Find each parasitized red blood cell.
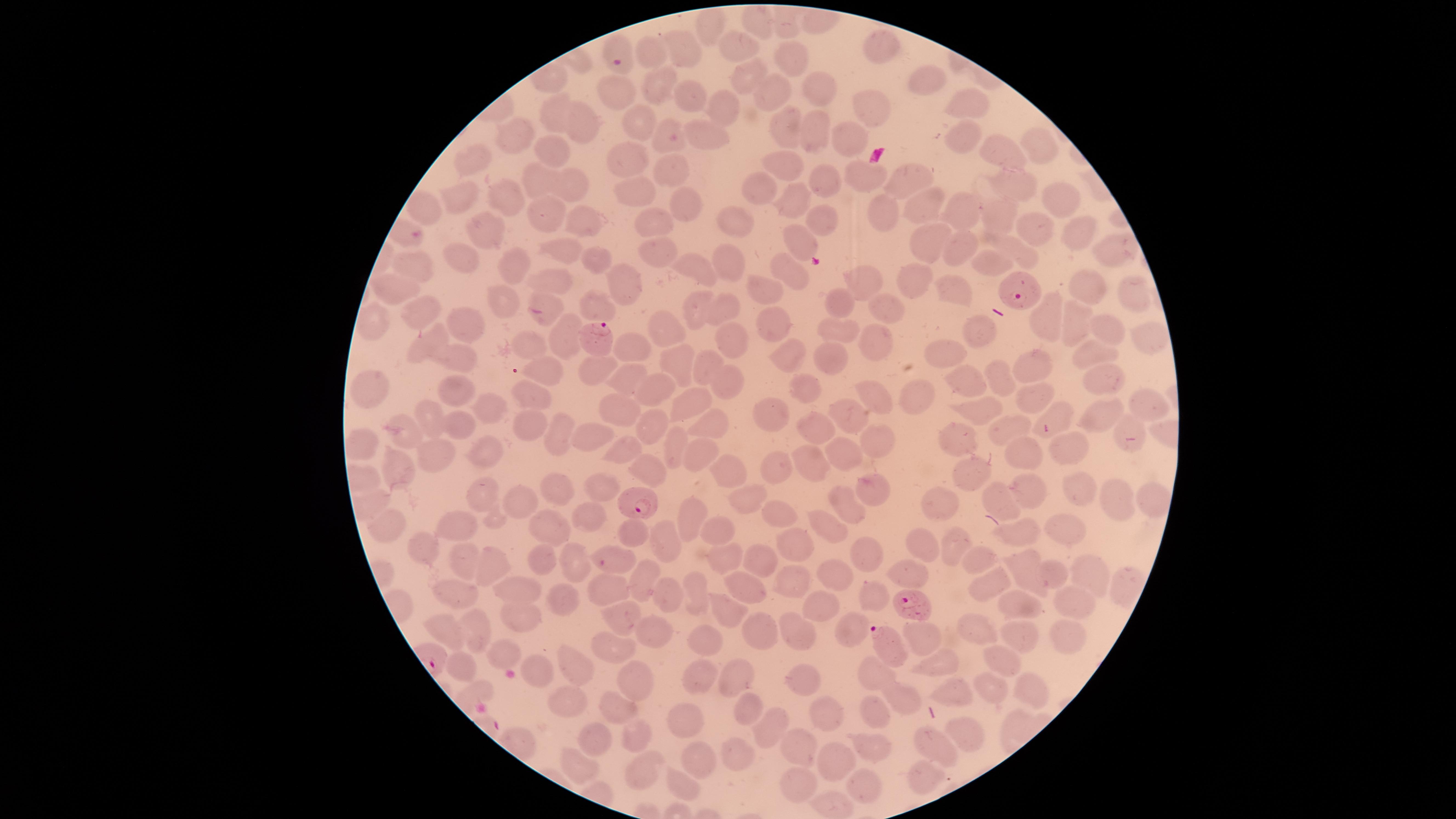

Approximate marker points as {x, y} in pixels.
Parasitized red blood cells: {621, 57}, {1019, 291}, {602, 335}, {643, 506}, {913, 602}, {883, 642}.

preparation: thin smear of blood
field_of_view: single
visible_region: circular
stain: Giemsa
image_size: 1456×819 pixels
species: Plasmodium falciparum
uninfected_red_blood_cells: 'approximate marker points as {x, y} in pixels: {760, 23}, {708, 24}, {734, 44}, {678, 48}, {876, 49}, {655, 56}, {792, 56}, {744, 77}, {658, 79}, {918, 81}, {774, 87}, {821, 90}, {615, 93}, {687, 99}, {721, 105}, {971, 105}, {549, 111}, {875, 113}, {584, 125}, {638, 126}, {784, 126}, {815, 132}, {518, 135}, {670, 135}, {705, 135}, {846, 140}, {962, 142}, {1043, 148}, {551, 150}, {1002, 151}, {472, 156}, {631, 157}, {671, 165}, {779, 165}, {861, 172}, {908, 173}, {1012, 179}, {535, 180}, {575, 182}, {825, 183}, {757, 189}, {640, 192}, {685, 195}, {503, 197}, {466, 198}, {796, 198}, {1057, 202}, {424, 207}, {925, 208}, {962, 210}, {884, 215}, {552, 217}, {649, 218}, {996, 218}, {580, 222}, {823, 222}, {737, 224}, {479, 230}, {1032, 230}, {1078, 236}, {928, 241}, {960, 243}, {803, 244}, {1111, 247}, {463, 252}, {563, 252}, {1024, 252}, {661, 253}, {596, 256}, {729, 259}, {990, 259}, {509, 262}, {414, 266}, {693, 266}, {796, 270}, {553, 282}, {757, 282}, {915, 283}, {623, 284}, {401, 285}, {872, 285}, {1083, 285}, {952, 290}, {1126, 293}, {501, 300}, {418, 302}, {690, 302}, {837, 303}, {723, 304}, {887, 309}, {595, 310}, {547, 312}, {1048, 314}, {369, 322}, {464, 323}, {775, 324}, {1073, 324}, {1110, 327}, {661, 330}, {839, 331}, {975, 333}, {563, 334}, {725, 334}, {875, 337}, {1147, 337}, {424, 340}, {528, 342}, {629, 345}, {1088, 349}, {791, 355}, {943, 355}, {459, 358}, {832, 359}, {681, 363}, {702, 364}, {1031, 364}, {593, 365}, {545, 366}, {1099, 375}, {626, 376}, {729, 379}, {999, 379}, {964, 385}, {368, 387}, {655, 387}, {805, 388}, {455, 391}, {529, 393}, {918, 394}, {878, 401}, {1032, 402}, {484, 405}, {1151, 405}, {682, 406}, {616, 407}, {985, 408}, {770, 409}, {1055, 411}, {1103, 413}, {427, 415}, {847, 418}, {530, 422}, {453, 425}, {648, 425}, {715, 426}, {814, 426}, {1007, 428}, {1129, 428}, {561, 430}, {588, 431}, {404, 435}, {956, 439}, {874, 442}, {354, 444}, {483, 445}, {670, 447}, {1071, 449}, {628, 450}, {838, 452}, {689, 454}, {425, 455}, {1023, 455}, {808, 458}, {393, 466}, {730, 468}, {779, 468}, {648, 469}, {970, 471}, {597, 479}, {557, 489}, {870, 490}, {1031, 490}, {1073, 490}, {1113, 493}, {477, 496}, {743, 497}, {521, 498}, {996, 499}, {1151, 502}, {846, 505}, {590, 511}, {774, 512}, {943, 513}, {689, 519}, {545, 522}, {460, 526}, {721, 527}, {825, 527}, {1059, 527}, {384, 528}, {1018, 531}, {632, 532}, {669, 538}, {423, 544}, {796, 544}, {926, 544}, {953, 547}, {863, 549}, {537, 551}, {612, 551}, {1023, 554}, {731, 558}, {981, 559}, {465, 560}, {765, 562}, {490, 565}, {571, 565}, {911, 570}, {1090, 572}, {1052, 573}, {784, 576}, {834, 577}, {643, 578}, {983, 578}, {1025, 578}, {745, 583}, {1120, 585}, {698, 587}, {606, 588}, {461, 590}, {519, 590}, {660, 591}, {871, 591}, {558, 598}, {1070, 598}, {1014, 601}, {722, 608}, {822, 608}, {621, 614}, {519, 616}, {976, 627}, {752, 628}, {441, 629}, {469, 630}, {650, 630}, {846, 630}, {1071, 633}, {800, 634}, {923, 636}, {1023, 636}, {613, 646}, {707, 646}, {500, 652}, {574, 657}, {932, 660}, {1001, 660}, {464, 670}, {538, 673}, {730, 676}, {877, 676}, {701, 677}, {631, 679}, {807, 680}, {991, 684}, {1024, 688}, {953, 691}, {567, 695}, {901, 698}, {752, 707}, {871, 712}, {618, 713}, {822, 713}, {679, 720}, {632, 729}, {775, 731}, {966, 731}, {593, 739}, {798, 743}, {934, 743}, {873, 748}, {733, 752}, {829, 753}, {700, 757}, {577, 768}, {640, 774}, {923, 775}, {678, 782}, {798, 782}, {866, 789}, {835, 806}'
capture: smartphone photograph through the microscope eyepiece